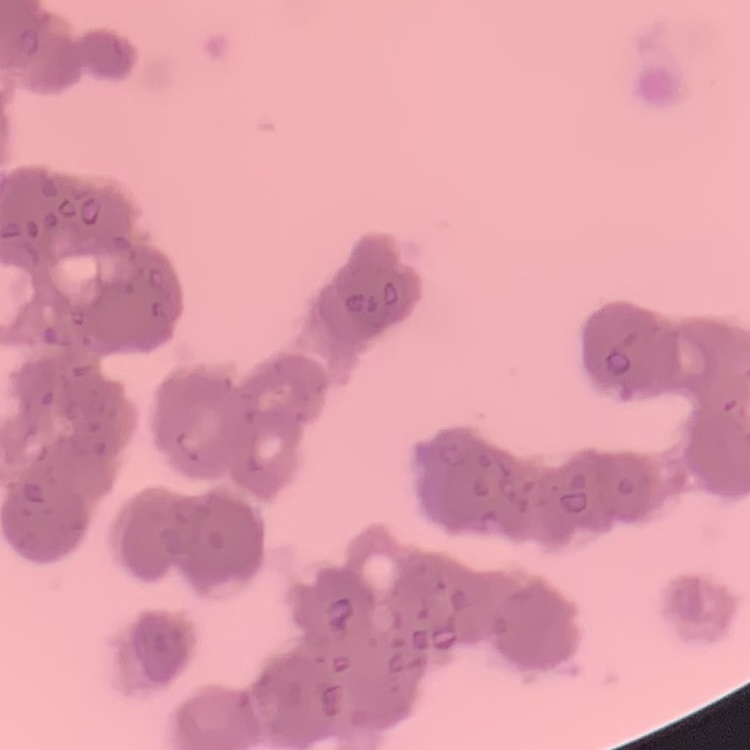

red_blood_cell_morphology: rouleaux formation
image_type: one tile cut from a larger photomicrograph
preparation: thin peripheral smear
stain: Field's or Giemsa